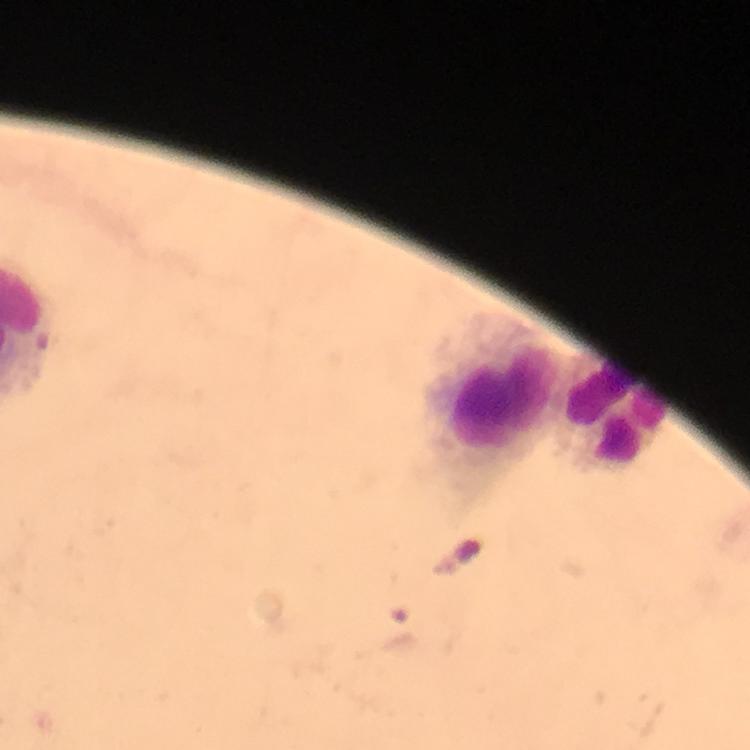

Approximate centers as (x, y) in pixels.
Summary:
  - Leukocyte locations: (488, 398), (611, 413)
  - Stain: Giemsa
  - Context: from a diagnostic examination for malaria
  - Cropped from: a single field of view
  - Plasmodium parasites: none seen
  - Immersion oil: used
  - Capture: smartphone camera through the microscope
  - Image size: 750×750 pixels
  - Preparation: thick blood smear
  - Magnification: 100x